Classify this cell by malaria status.
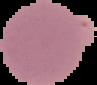

Uninfected.

From a thin blood film. Cell region segmented out of the field of view; the surrounding area is masked to black. Image is 97×85 pixels.